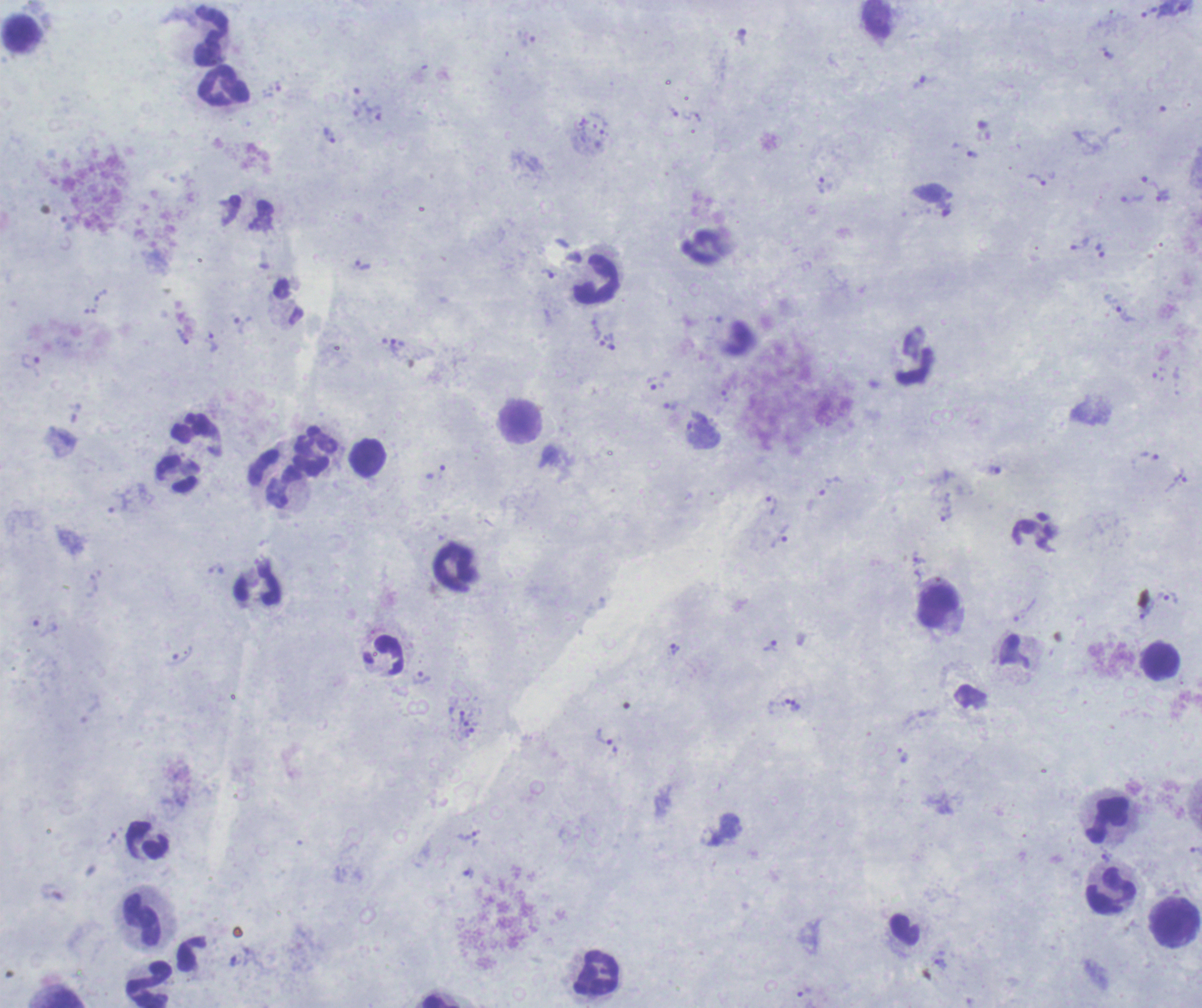 Romanowsky-stained preparation. One field from this slide. Thick blood film. Image is 1202×1008 pixels.